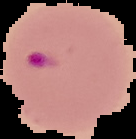

preparation = thin blood smear
image size = 136×139 pixels
image type = segmented cell region on a black background
result = Plasmodium parasites identified